Name the parasite shown.
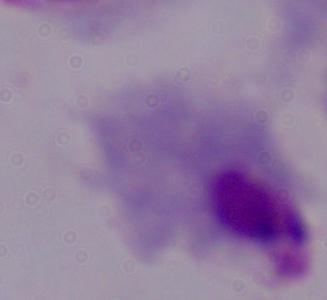
This is a trichomonad.

Summary:
  - Modality: photomicrograph
  - Magnification: 1000x